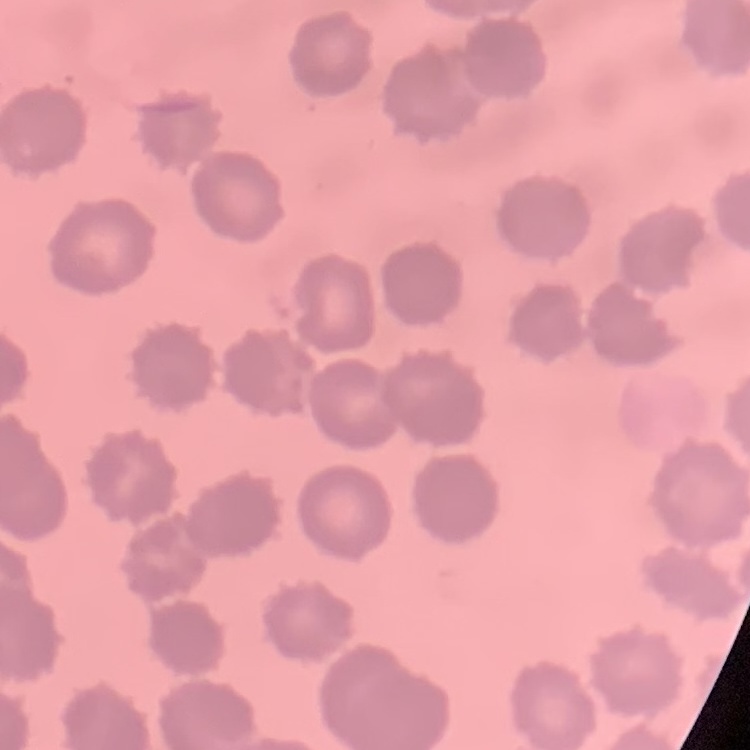

erythrocyte_morphology: no rouleaux formation
preparation: thin peripheral smear
image_type: one tile cut from a larger photomicrograph
stain: Field's or Giemsa